Name the blood parasite species.
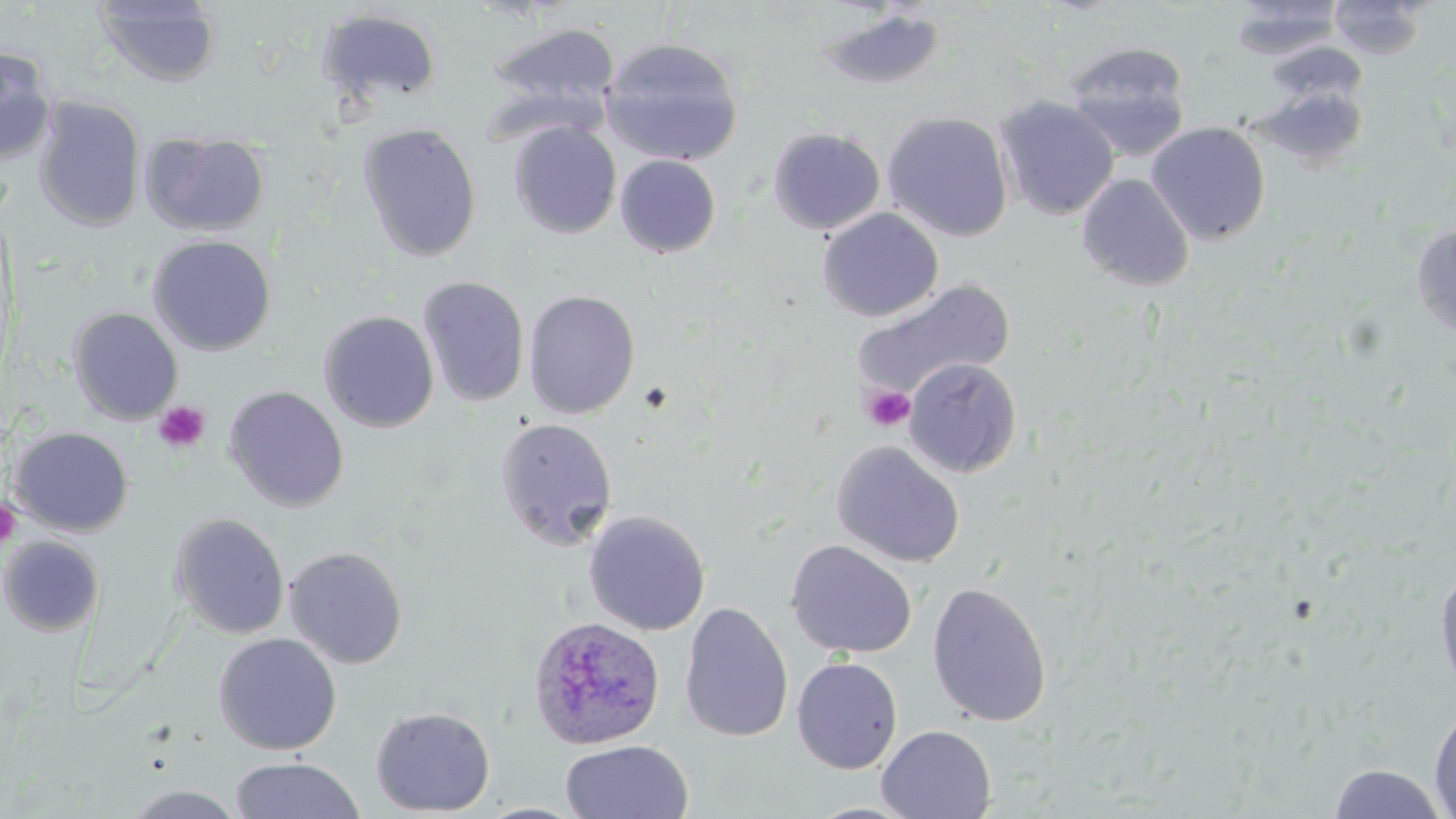

Plasmodium ovale.

Summary:
  - Coordinate format: approximate bounding boxes as [x1, y1, x2, y2] in pixels
  - Uninfected red blood cell locations: [92, 0, 222, 88], [1229, 0, 1346, 59], [1329, 0, 1427, 58], [814, 7, 948, 91], [316, 8, 443, 110], [483, 21, 621, 123], [481, 27, 732, 145], [599, 37, 745, 167], [1264, 41, 1369, 108], [1061, 42, 1193, 159], [0, 46, 57, 165], [1249, 86, 1369, 170], [33, 96, 146, 231], [994, 96, 1120, 221], [882, 111, 1013, 242], [1146, 121, 1271, 245], [357, 122, 483, 264], [509, 122, 621, 239], [768, 127, 885, 235], [141, 131, 270, 237], [614, 155, 722, 258], [1076, 173, 1195, 292], [817, 208, 943, 322], [1411, 224, 1456, 340], [148, 235, 277, 356], [417, 276, 530, 408], [851, 280, 1015, 402], [523, 289, 641, 420], [68, 307, 184, 425], [318, 310, 439, 432], [902, 357, 1023, 478], [223, 385, 349, 513], [494, 417, 618, 552], [10, 426, 134, 537], [831, 441, 965, 568], [583, 510, 710, 636], [169, 512, 290, 640], [0, 536, 104, 637], [786, 539, 918, 659], [284, 545, 409, 669], [1434, 565, 1456, 696], [927, 580, 1053, 727], [679, 602, 794, 742], [213, 633, 342, 755], [791, 656, 903, 774], [1428, 703, 1456, 817], [370, 706, 496, 816], [876, 725, 996, 819], [559, 740, 693, 819], [229, 757, 366, 819], [1326, 763, 1451, 819], [122, 785, 248, 818], [803, 801, 924, 818]
  - Platelet locations: [637, 380, 675, 415], [861, 385, 916, 433], [154, 401, 210, 454], [0, 498, 21, 550]
  - Plasmodium ovale-infected red blood cell locations: [528, 615, 665, 749]
  - Field of view: single
  - Modality: light microscopy
  - Preparation: thin blood smear
  - Stain: May-Grünwald-Giemsa
  - Magnification: 1000x
  - Image size: 1456×819 pixels